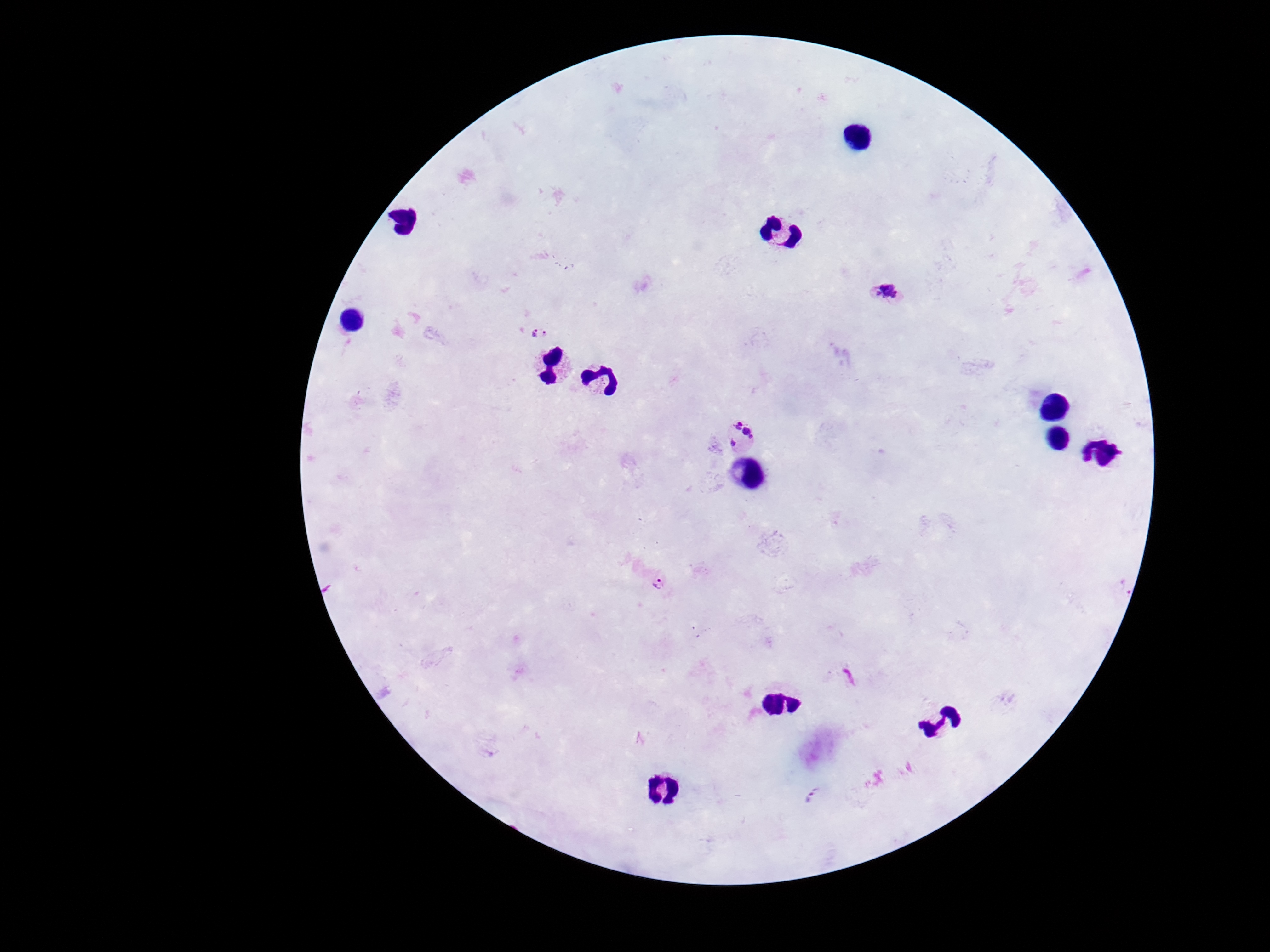

Approximate centers as (x, y) in pixels. Plasmodium parasite locations: (888, 293), (539, 334), (740, 437), (659, 579), (812, 795). Image is 1270×952 pixels. 100x magnification. One field from this slide. Patient malaria status: infected. Giemsa stain. Smartphone photograph taken through the microscope eyepiece. Thick blood film.